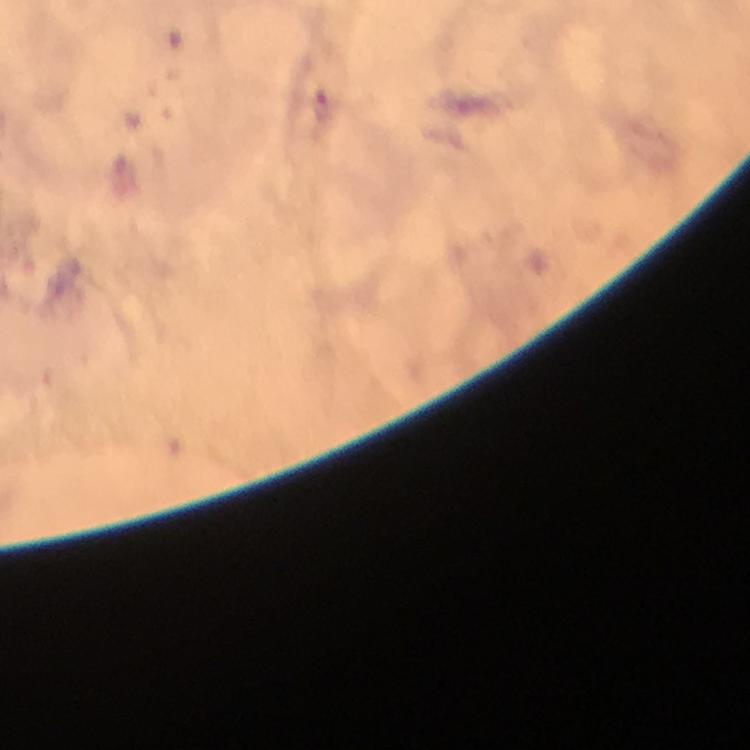 Approximate centers as [x, y] in pixels. Plasmodium parasite locations: [321, 106]. A crop from one field of view. Image is 750×750 pixels. 100x magnification. Photographed with a smartphone mounted on the microscope. Giemsa stain. Thick blood film. Immersion oil applied. From a diagnostic examination for malaria.